Report the malaria status of this cell.
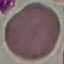

It is uninfected.

stain: Giemsa
image_type: cell patch, automatically extracted from a larger field of view and resized to 64 × 64 pixels
capture: smartphone through the microscope eyepiece
preparation: thin blood smear